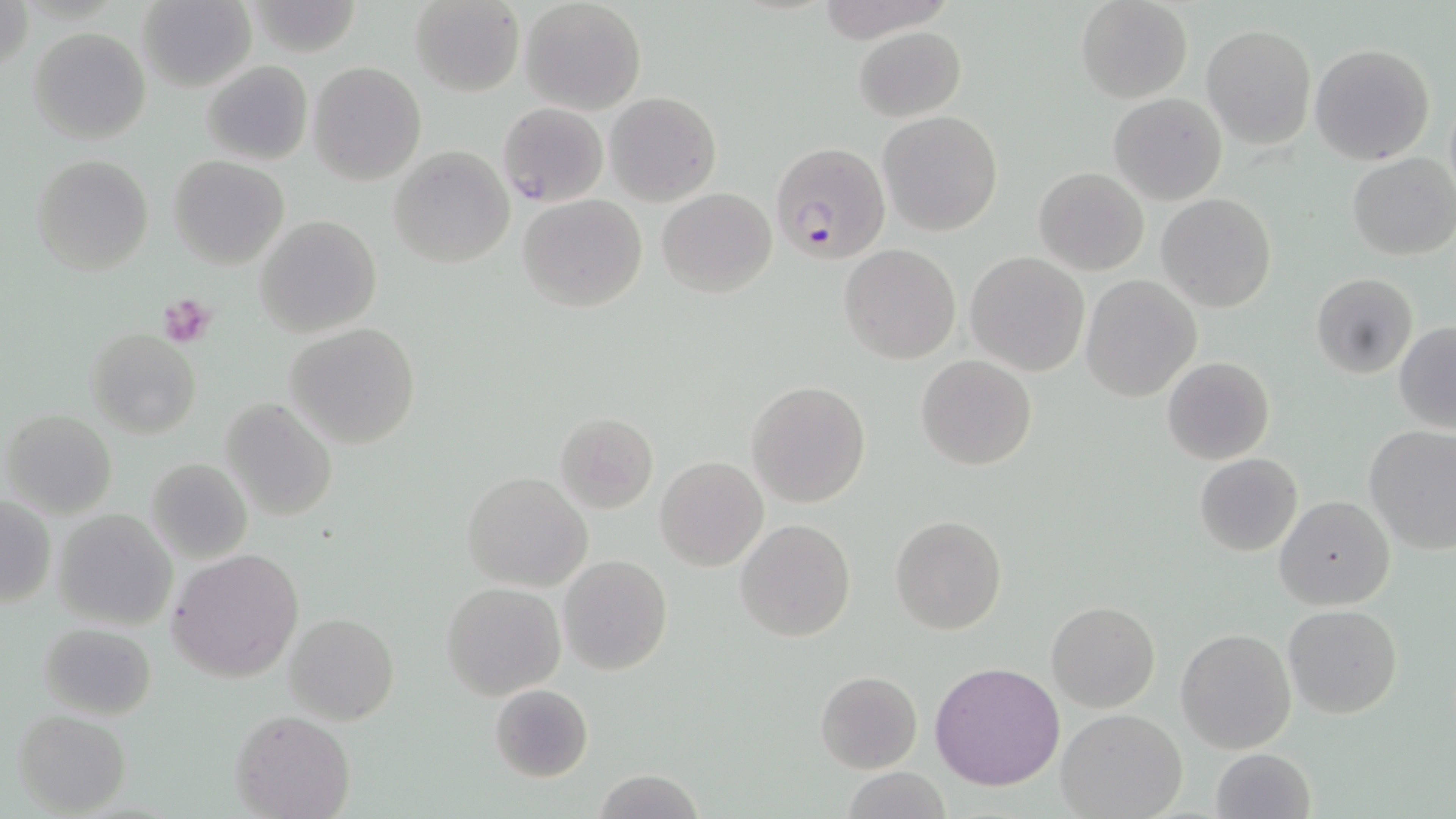
Summary:
  - Coordinate format: approximate bounding boxes as (x1,y1)-(x2,y2) corner pairs in pixels
  - Platelet locations: (159,295)-(217,346)
  - Uninfected red blood cell locations: (1,0)-(29,77), (519,0)-(647,114), (1076,0)-(1194,103), (136,1)-(256,91), (245,1)-(365,56), (409,1)-(526,96), (1202,25)-(1315,148), (853,26)-(966,122), (30,28)-(150,143), (1309,43)-(1436,165), (202,59)-(313,165), (308,60)-(426,185), (605,92)-(720,204), (1108,92)-(1227,204), (497,102)-(608,207), (877,111)-(1003,237), (388,146)-(514,269), (1348,153)-(1455,261), (32,154)-(155,275), (169,156)-(290,270), (1032,167)-(1149,276), (656,187)-(776,297), (518,193)-(647,313), (1157,193)-(1276,312), (254,215)-(382,337), (840,244)-(962,365), (964,252)-(1090,376), (1311,272)-(1419,379), (1081,275)-(1202,401), (285,322)-(420,448), (1394,322)-(1456,433), (84,327)-(202,439), (916,355)-(1038,472), (1162,356)-(1274,464), (745,379)-(873,508), (221,397)-(337,521), (3,409)-(117,519), (554,411)-(658,513), (1363,426)-(1456,555), (1194,454)-(1303,556), (146,457)-(253,563), (655,457)-(769,572), (463,471)-(592,592), (0,495)-(55,609), (1274,495)-(1395,611), (52,508)-(178,631), (890,514)-(1007,634), (735,518)-(856,643), (168,548)-(304,683), (557,554)-(672,676), (441,581)-(565,698), (1047,599)-(1160,712), (1283,603)-(1402,718), (285,613)-(399,725), (39,621)-(157,720), (1175,627)-(1296,755), (929,660)-(1065,791), (815,671)-(922,773), (488,684)-(594,783), (1056,709)-(1187,818), (13,710)-(131,816), (232,710)-(355,819), (1209,748)-(1314,819), (589,769)-(705,819), (842,770)-(953,818)
  - Plasmodium falciparum-infected red blood cell locations: (770,141)-(891,265)
  - Slide-level diagnosis: Plasmodium falciparum
  - Field of view: one of a larger specimen
  - Stain: May-Grünwald-Giemsa
  - Preparation: thin blood film
  - Magnification: 1000x
  - Modality: light microscopy
  - Image size: 1456×819 pixels